Give the position of every leukocyte visible.
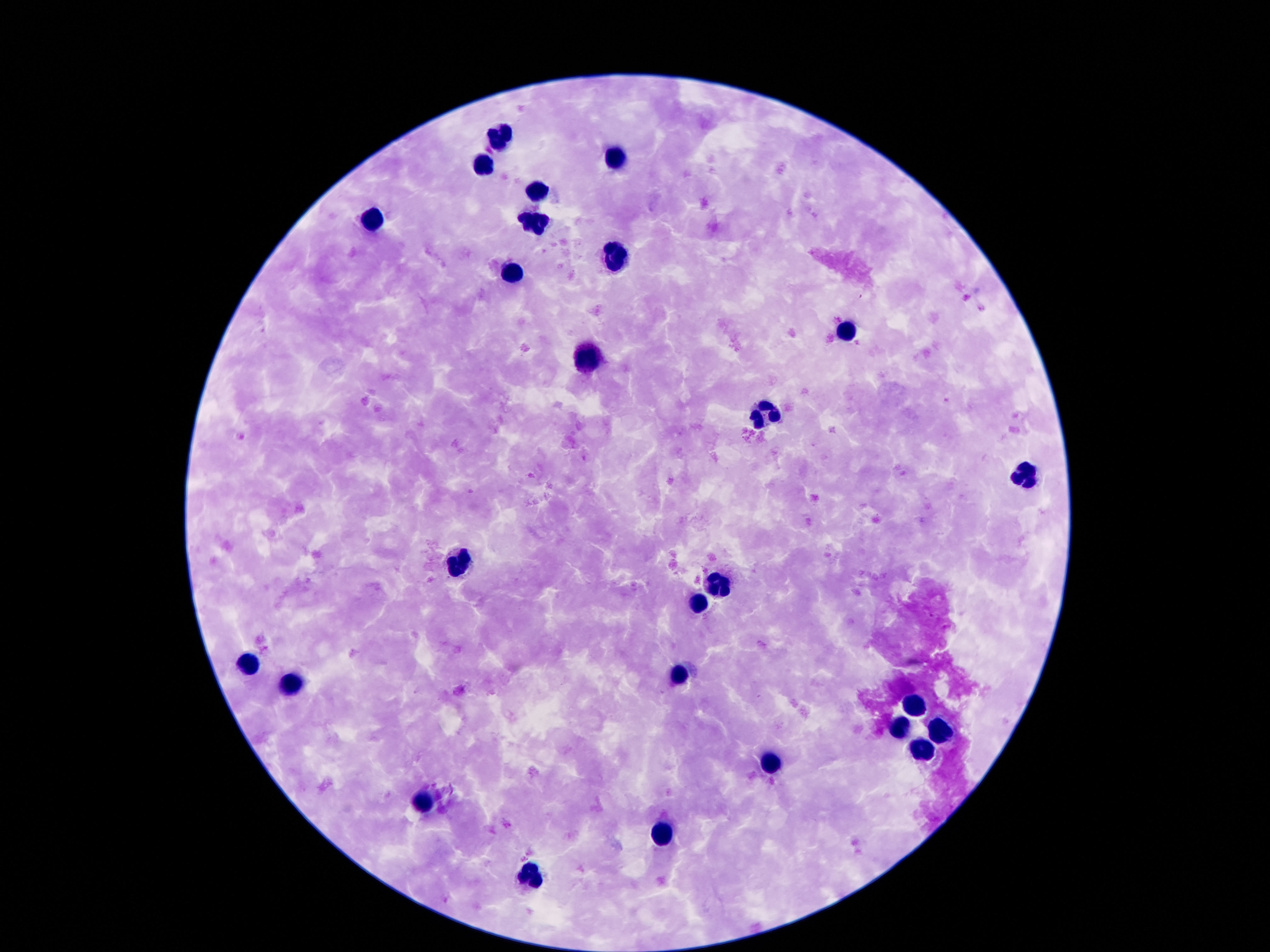

Approximate object centers, in pixels from the top-left corner.
Leukocytes: (x=499, y=136), (x=614, y=160), (x=484, y=162), (x=535, y=189), (x=371, y=218), (x=532, y=218), (x=614, y=258), (x=511, y=270), (x=847, y=330), (x=588, y=361), (x=763, y=414), (x=1022, y=479), (x=458, y=570), (x=720, y=580), (x=698, y=603), (x=247, y=665), (x=678, y=675), (x=287, y=682), (x=909, y=702), (x=936, y=733), (x=900, y=735), (x=921, y=746), (x=770, y=760), (x=426, y=810), (x=661, y=835), (x=531, y=877).

Summary:
  - Patient malaria status: negative
  - Stain: Giemsa
  - Preparation: thick blood film
  - Capture: smartphone camera through the microscope eyepiece
  - Image size: 1270×952 pixels
  - Magnification: 100x
  - Field of view: single